Assess this cell for malaria.
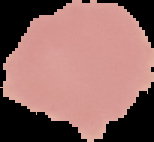

It is uninfected.

Summary:
  - Image size: 154×142 pixels
  - Preparation: thin blood film
  - Image type: segmented cell region with the area outside set to black